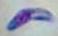
Summary:
  - Identification: Toxoplasma gondii
  - Magnification: 1000x
  - Modality: micrograph